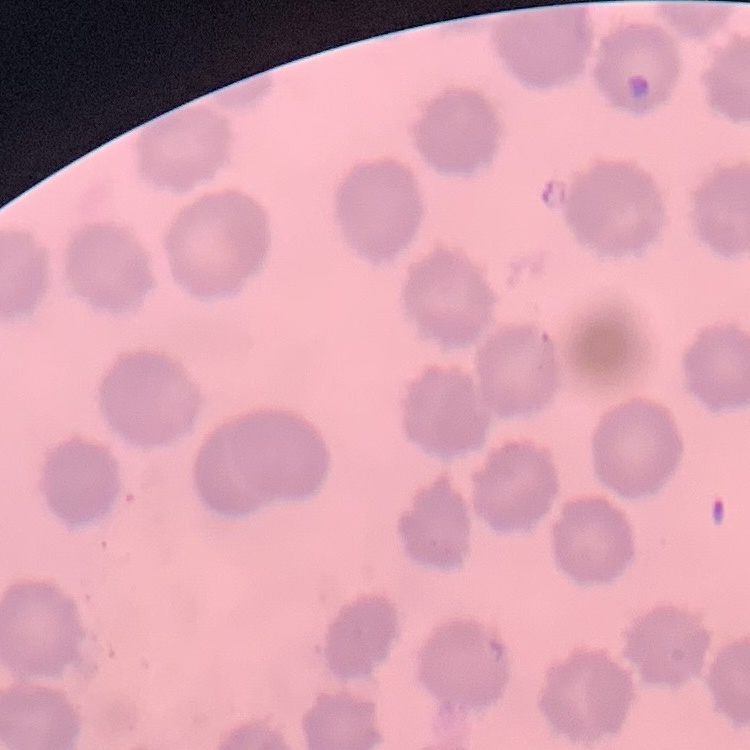

The erythrocytes show no rouleaux formation. One tile cut from a larger photomicrograph. Thin blood film. Field's or Giemsa stain.